Identify the cell.
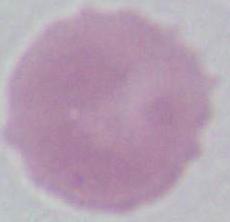

This is an erythrocyte.

1000x magnification. Photomicrograph.